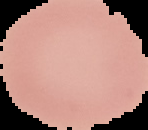 Malaria status: uninfected. Cell region segmented out of the field of view; the surrounding area is masked to black. From a thin blood smear. Image is 148×130 pixels.